Locate every P. falciparum parasite and identify its life-cycle stage.
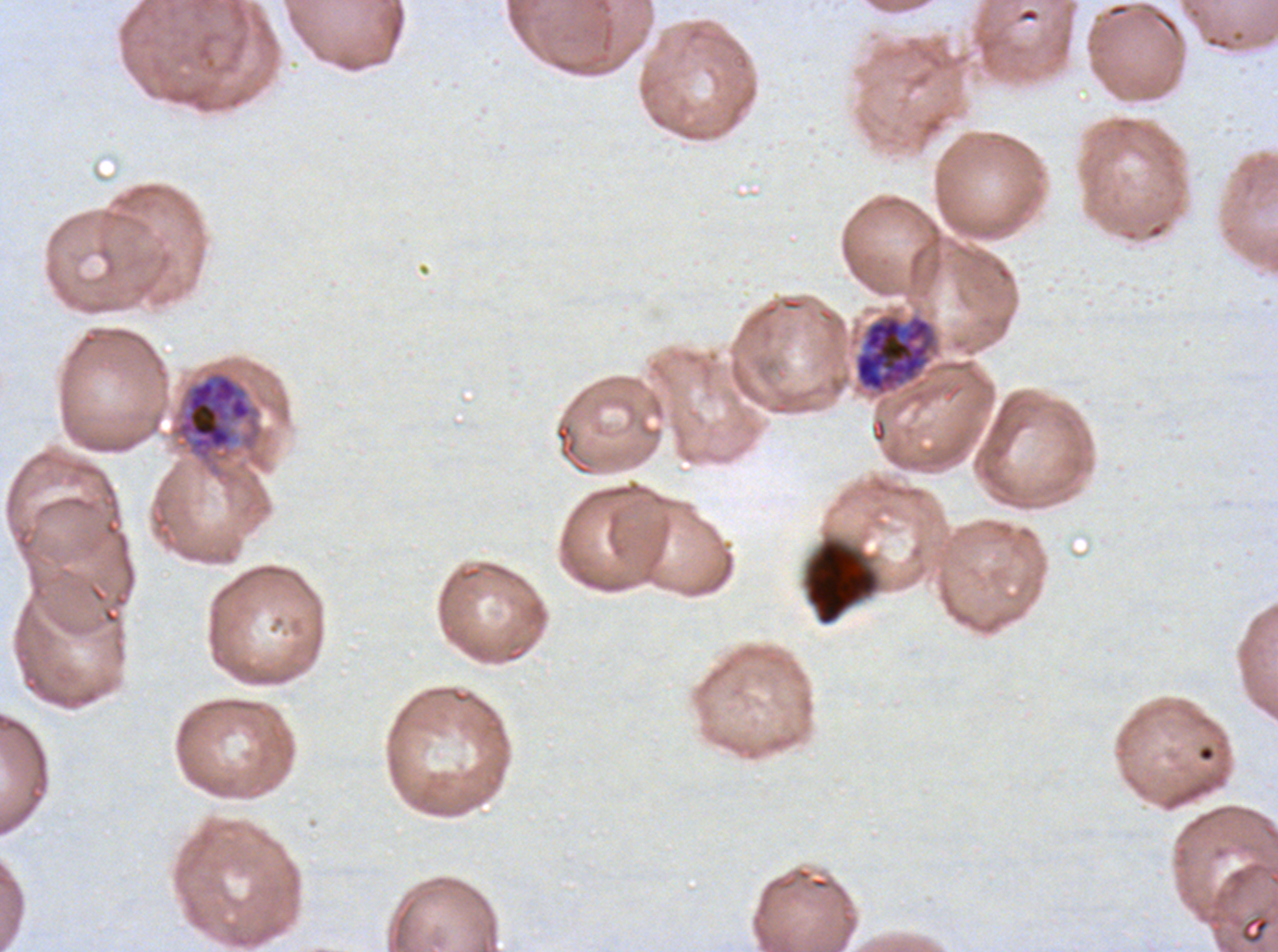

Approximate bounding boxes as [x1, y1, x2, y2] in pixels.
Early schizonts: [854, 314, 937, 396], [170, 369, 264, 466].
No rings, late-ring/early-trophozoite forms, mid trophozoites, late trophozoites, late schizonts, segmenters, or gametocytes observed.

Summary:
  - Debris locations: [804, 538, 879, 626]
  - Image size: 1278×952 pixels
  - Specimen: ex-vivo P. falciparum culture from a patient in The Gambia, grown for 24 to 48 hours
  - Field of view: sub-image separated from a larger composite
  - Preparation: thin blood film
  - Stain: Giemsa